State the blood parasite species.
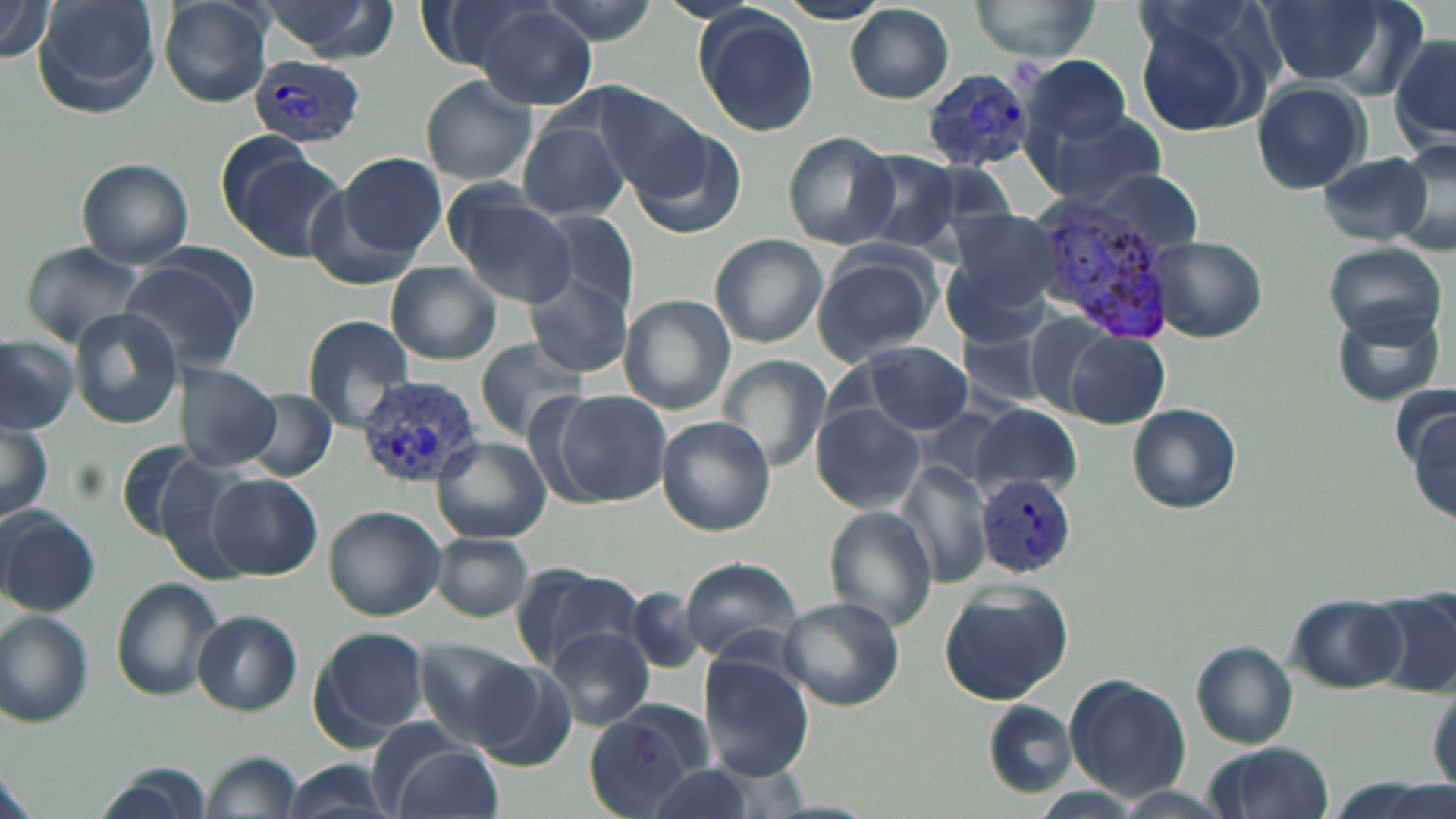

Plasmodium vivax.

uninfected red blood cell locations = approximate bounding boxes as (x1,y1)-(x2,y2) corner pairs in pixels: (36,0)-(163,108), (417,0)-(551,75), (534,0)-(662,44), (968,0)-(1104,60), (1255,0)-(1404,89), (0,1)-(55,60), (157,1)-(273,108), (256,1)-(400,61), (779,1)-(890,24), (464,5)-(597,108), (846,5)-(956,104), (691,7)-(821,139), (1129,8)-(1274,138), (1391,36)-(1456,148), (1022,54)-(1131,145), (421,77)-(538,185), (1252,79)-(1372,192), (595,90)-(716,206), (1034,111)-(1170,209), (517,119)-(630,223), (624,126)-(748,241), (783,132)-(899,251), (1387,136)-(1456,258), (221,142)-(344,258), (854,149)-(963,254), (337,152)-(447,261), (1315,153)-(1434,245), (76,158)-(194,267), (1085,168)-(1206,258), (446,189)-(580,307), (533,208)-(641,315), (941,218)-(1060,343), (710,233)-(827,348), (1147,236)-(1267,342), (24,243)-(143,344), (1320,243)-(1447,343), (811,248)-(940,364), (116,257)-(254,372), (385,262)-(502,365), (523,271)-(632,378), (620,294)-(736,414), (1327,302)-(1449,408), (69,306)-(184,428), (1020,311)-(1125,417), (302,315)-(415,430), (958,324)-(1054,410), (1063,329)-(1171,430), (0,335)-(78,433), (475,340)-(588,438), (854,341)-(974,435), (719,355)-(832,473), (172,363)-(281,470), (246,389)-(338,481), (544,389)-(671,506), (1128,402)-(1242,513), (812,404)-(925,513), (915,405)-(1019,493), (971,405)-(1080,496), (1410,410)-(1454,524), (0,417)-(54,523), (656,417)-(777,535), (434,436)-(550,544), (147,455)-(254,583), (900,460)-(993,586), (206,473)-(322,580), (324,505)-(446,621), (825,506)-(939,631), (0,508)-(100,616), (802,530)-(925,684), (431,533)-(534,622), (679,556)-(804,664), (509,562)-(644,674), (111,579)-(224,702), (939,583)-(1072,704), (624,585)-(709,673), (1373,590)-(1456,697), (1287,593)-(1408,692), (779,597)-(905,710), (1,611)-(95,727), (192,611)-(301,715), (309,625)-(431,744), (549,627)-(653,730), (415,638)-(537,747), (1191,640)-(1298,746), (699,653)-(814,781), (468,661)-(578,770), (1064,673)-(1193,800), (1428,678)-(1456,798), (983,701)-(1073,796), (582,703)-(713,817), (382,740)-(505,819), (1202,742)-(1336,819), (206,751)-(300,818), (281,760)-(397,819), (645,765)-(760,818), (96,767)-(208,816)
image size = 1456×819 pixels
stain = May-Grünwald-Giemsa
Plasmodium vivax-infected red blood cell locations = approximate bounding boxes as (x1,y1)-(x2,y2) corner pairs in pixels: (248,53)-(368,148), (917,70)-(1033,174), (1027,194)-(1180,346), (355,375)-(482,488), (978,476)-(1077,578)
modality = light microscopy
preparation = thin blood smear
field of view = single
magnification = 1000x